Locate and identify every blood parasite.
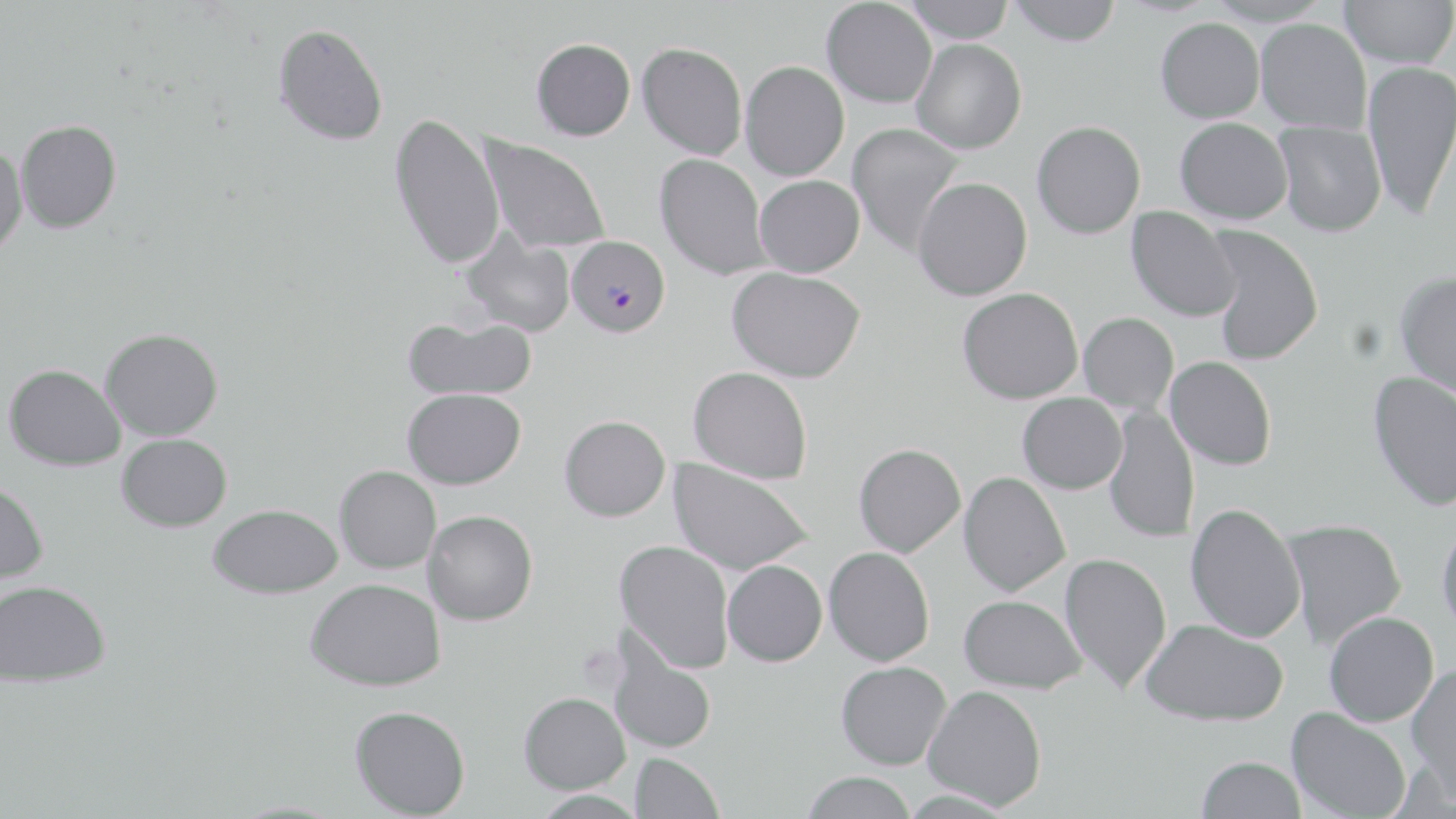

Approximate bounding boxes as (x1,y1)-(x2,y2) corner pairs in pixels.
Plasmodium falciparum-infected red blood cells: (566,235)-(670,337).
No Plasmodium ovale, Plasmodium malariae, Plasmodium vivax, Babesia divergens, or Trypanosoma brucei observed.

slide-level diagnosis = Plasmodium falciparum
stain = May-Grünwald-Giemsa
modality = optical microscopy
uninfected red blood cell locations = approximate bounding boxes as (x1,y1)-(x2,y2) corner pairs in pixels: (903,0)-(1017,42), (1008,0)-(1121,46), (1206,0)-(1333,27), (1339,0)-(1455,68), (821,1)-(937,108), (1155,17)-(1264,123), (1255,19)-(1372,133), (273,22)-(389,147), (531,38)-(635,141), (911,38)-(1027,154), (637,42)-(747,160), (1362,60)-(1456,221), (740,61)-(850,180), (389,111)-(506,270), (1174,117)-(1292,225), (16,120)-(122,233), (1273,120)-(1386,237), (1031,121)-(1146,239), (847,122)-(966,258), (478,134)-(612,256), (0,144)-(27,260), (654,153)-(770,280), (754,174)-(865,277), (912,177)-(1032,301), (1126,207)-(1242,322), (1206,226)-(1323,365), (460,229)-(576,338), (727,266)-(865,383), (1395,271)-(1456,401), (957,287)-(1083,404), (1078,312)-(1179,414), (403,315)-(537,401), (100,328)-(223,441), (1164,356)-(1277,470), (4,364)-(125,471), (688,366)-(813,485), (1367,371)-(1456,511), (402,388)-(526,489), (1017,392)-(1127,494), (1104,406)-(1199,543), (559,415)-(671,521), (116,434)-(232,532), (853,443)-(966,557), (668,458)-(814,577), (334,465)-(441,574), (958,471)-(1070,597), (0,481)-(49,586), (1185,502)-(1306,644), (208,504)-(343,599), (422,510)-(538,625), (1279,518)-(1407,650), (1436,518)-(1456,639), (614,539)-(734,672), (823,547)-(935,666), (1059,552)-(1172,693), (722,560)-(827,666), (305,578)-(446,691), (0,580)-(111,687), (958,594)-(1087,693), (1323,612)-(1439,726), (1139,618)-(1288,726), (606,636)-(717,754), (835,661)-(951,770), (1406,663)-(1456,801), (923,684)-(1047,811), (518,692)-(630,794), (349,705)-(470,818), (1286,707)-(1412,819), (630,752)-(724,818), (1196,755)-(1305,818), (800,771)-(917,819), (531,789)-(647,818)
image size = 1456×819 pixels
preparation = thin blood smear
magnification = 1000x
field of view = single